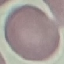

Summary:
  - Result: no malaria parasites seen
  - Image type: automatically extracted cell patch, resized to 64 × 64 pixels
  - Capture: smartphone through the microscope eyepiece
  - Stain: Giemsa
  - Preparation: thin smear